State which parasite is depicted.
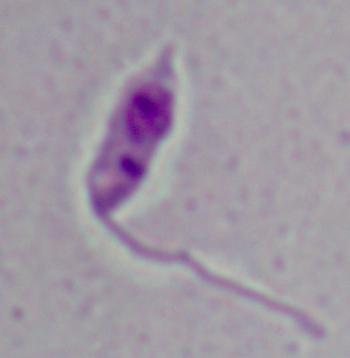

Leishmania.

Summary:
  - Magnification: 1000x
  - Modality: micrograph